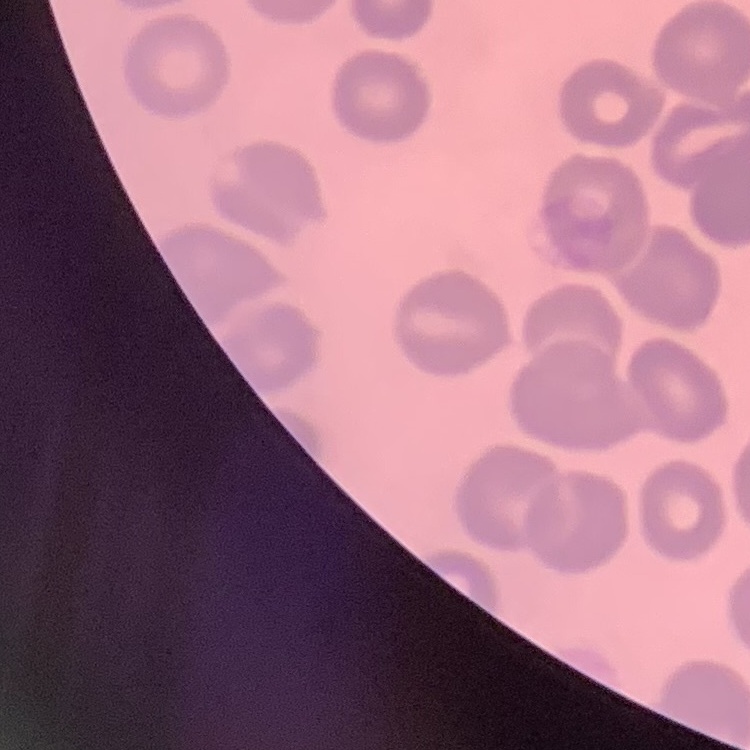

Summary:
  - Red blood cell morphology: no rouleaux formation
  - Preparation: thin blood smear
  - Image type: one tile cut from a larger photomicrograph
  - Stain: Field's or Giemsa